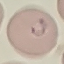

{
  "malaria_status": "parasitized",
  "preparation": "thin blood film",
  "capture": "smartphone camera at the microscope eyepiece",
  "stain": "Giemsa",
  "image_type": "automatically extracted cell patch, resized to 64 × 64 pixels"
}